Outline each Plasmodium malariae-infected red blood cell.
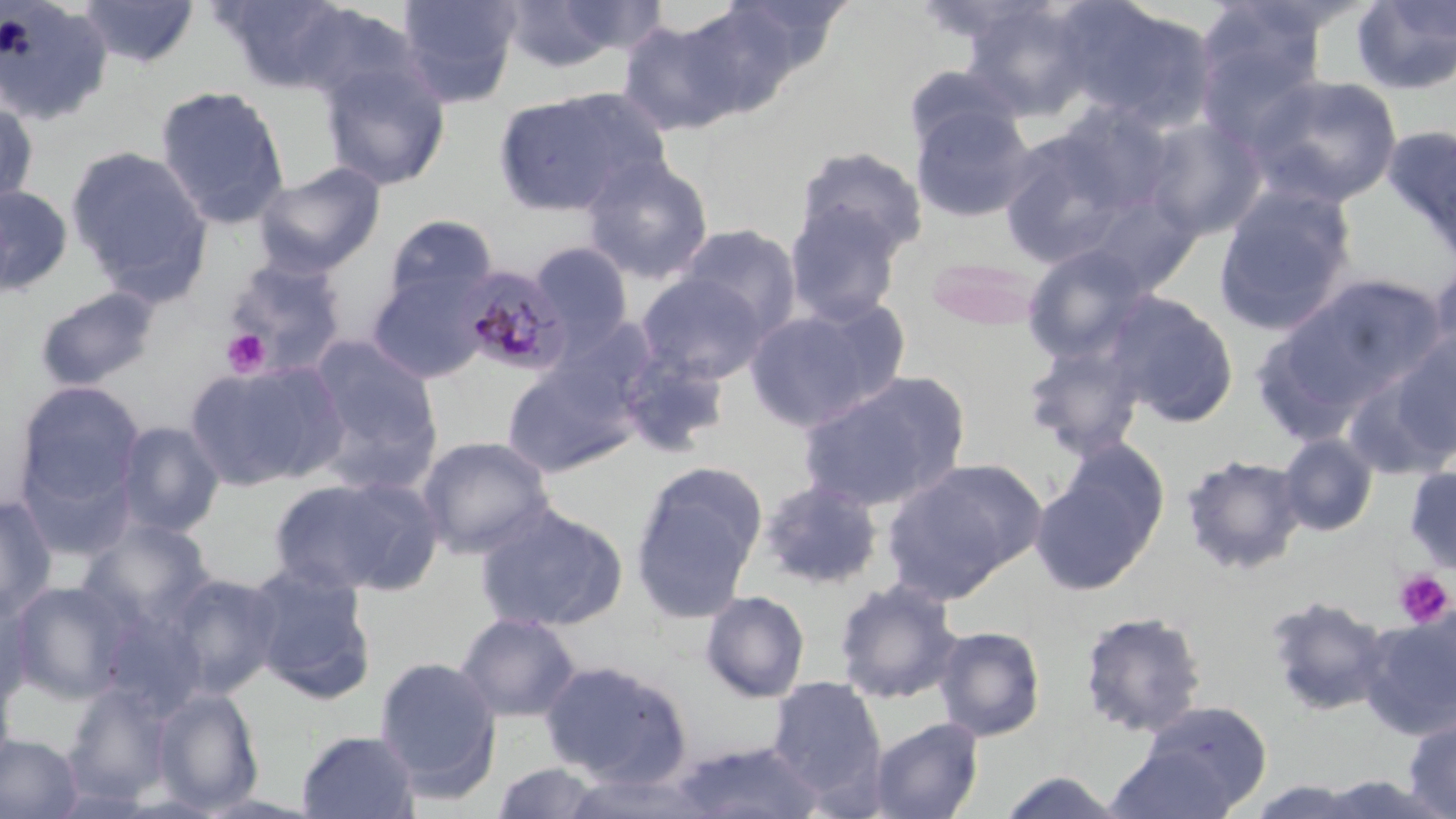
Approximate bounding boxes as named x1/y1/x2/y2 corners in pixels.
Plasmodium malariae-infected red blood cells: (x1=459, y1=265, x2=572, y2=377).

Uninfected red blood cell locations: (x1=78, y1=0, x2=200, y2=69), (x1=214, y1=0, x2=359, y2=93), (x1=396, y1=0, x2=521, y2=107), (x1=497, y1=0, x2=650, y2=73), (x1=1350, y1=0, x2=1456, y2=96), (x1=714, y1=1, x2=852, y2=80), (x1=0, y1=2, x2=113, y2=126), (x1=960, y1=2, x2=1098, y2=120), (x1=1063, y1=2, x2=1217, y2=134), (x1=673, y1=3, x2=807, y2=117), (x1=617, y1=16, x2=749, y2=136), (x1=319, y1=56, x2=451, y2=191), (x1=903, y1=64, x2=1024, y2=157), (x1=1247, y1=73, x2=1404, y2=209), (x1=154, y1=85, x2=289, y2=230), (x1=492, y1=89, x2=659, y2=219), (x1=0, y1=99, x2=39, y2=207), (x1=911, y1=103, x2=1036, y2=224), (x1=1141, y1=116, x2=1266, y2=241), (x1=1382, y1=124, x2=1456, y2=263), (x1=998, y1=128, x2=1134, y2=269), (x1=66, y1=145, x2=213, y2=301), (x1=794, y1=146, x2=928, y2=261), (x1=582, y1=155, x2=715, y2=284), (x1=252, y1=160, x2=387, y2=278), (x1=1213, y1=183, x2=1358, y2=338), (x1=0, y1=185, x2=73, y2=296), (x1=784, y1=206, x2=903, y2=326), (x1=383, y1=214, x2=498, y2=311), (x1=675, y1=224, x2=802, y2=340), (x1=529, y1=241, x2=634, y2=350), (x1=1020, y1=243, x2=1155, y2=364), (x1=925, y1=255, x2=1047, y2=332), (x1=224, y1=257, x2=348, y2=376), (x1=1425, y1=257, x2=1456, y2=380), (x1=367, y1=272, x2=487, y2=384), (x1=636, y1=272, x2=771, y2=383), (x1=1266, y1=274, x2=1448, y2=419), (x1=34, y1=285, x2=161, y2=393), (x1=1104, y1=291, x2=1240, y2=428), (x1=743, y1=300, x2=908, y2=434), (x1=1387, y1=330, x2=1456, y2=458), (x1=304, y1=335, x2=442, y2=481), (x1=1022, y1=341, x2=1147, y2=461), (x1=616, y1=350, x2=731, y2=458), (x1=185, y1=361, x2=344, y2=491), (x1=501, y1=361, x2=638, y2=478), (x1=1342, y1=367, x2=1455, y2=482), (x1=795, y1=371, x2=970, y2=514), (x1=14, y1=380, x2=146, y2=523), (x1=115, y1=421, x2=225, y2=538), (x1=1277, y1=434, x2=1378, y2=537), (x1=416, y1=435, x2=556, y2=560), (x1=1031, y1=444, x2=1168, y2=597), (x1=1181, y1=453, x2=1308, y2=577), (x1=882, y1=456, x2=1045, y2=599), (x1=629, y1=462, x2=766, y2=622), (x1=1404, y1=465, x2=1456, y2=576), (x1=268, y1=474, x2=443, y2=598), (x1=757, y1=479, x2=884, y2=591), (x1=0, y1=495, x2=56, y2=624), (x1=475, y1=502, x2=628, y2=633), (x1=78, y1=518, x2=215, y2=633), (x1=246, y1=564, x2=378, y2=704), (x1=162, y1=572, x2=284, y2=700), (x1=832, y1=577, x2=964, y2=705), (x1=9, y1=580, x2=135, y2=704), (x1=699, y1=590, x2=811, y2=703), (x1=0, y1=592, x2=36, y2=711), (x1=1264, y1=594, x2=1391, y2=718), (x1=98, y1=609, x2=208, y2=719), (x1=1078, y1=610, x2=1207, y2=738), (x1=1359, y1=610, x2=1456, y2=740), (x1=455, y1=611, x2=581, y2=723), (x1=933, y1=624, x2=1047, y2=742), (x1=373, y1=655, x2=502, y2=801), (x1=540, y1=659, x2=693, y2=785), (x1=0, y1=665, x2=16, y2=783), (x1=767, y1=675, x2=886, y2=797), (x1=64, y1=682, x2=172, y2=806), (x1=151, y1=687, x2=264, y2=814), (x1=1132, y1=700, x2=1273, y2=812), (x1=1403, y1=714, x2=1456, y2=818), (x1=867, y1=717, x2=984, y2=819), (x1=296, y1=729, x2=420, y2=818), (x1=0, y1=732, x2=84, y2=819), (x1=669, y1=741, x2=826, y2=818), (x1=1105, y1=745, x2=1241, y2=819), (x1=490, y1=762, x2=610, y2=818), (x1=558, y1=770, x2=719, y2=818), (x1=993, y1=770, x2=1128, y2=818). Platelet locations: (x1=221, y1=329, x2=271, y2=378), (x1=1393, y1=569, x2=1453, y2=628). Slide-level diagnosis: Plasmodium malariae. Single field of view. Light microscopy. Image is 1456×819 pixels. May-Grünwald-Giemsa-stained preparation. Captured at 1000x magnification. Thin blood smear.